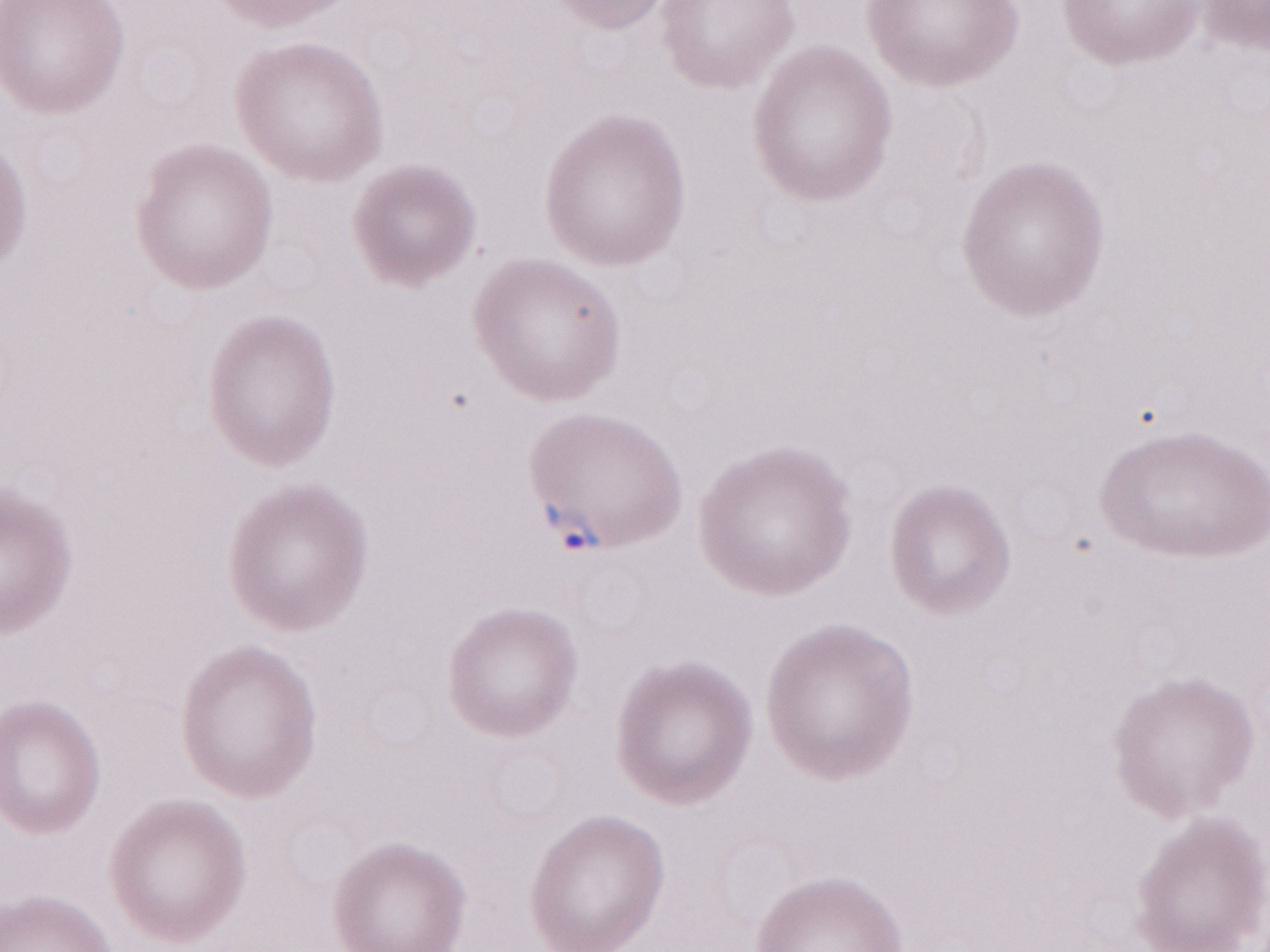 Olympus BX43 microscope and DP73 digital camera. Single field of view. May-Grünwald-Giemsa-stained preparation. Thin peripheral-blood smear. Image is 1270×952 pixels. Patient-level malaria diagnosis: positive. 1,000x magnification.